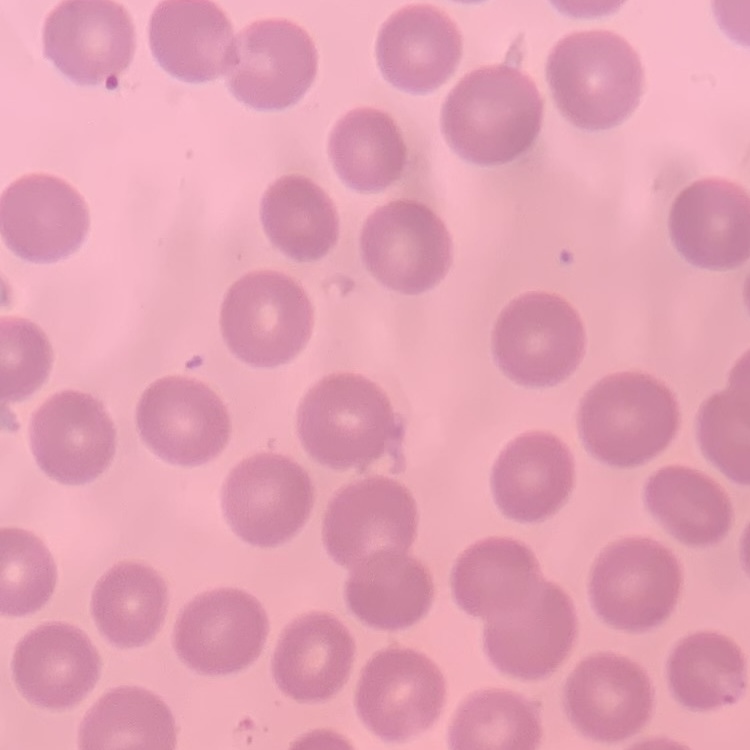

erythrocyte_morphology: no rouleaux formation
image_type: one tile cut from a larger photomicrograph
preparation: thin blood film
stain: Field's or Giemsa